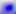

Summary:
  - Identification: Toxoplasma gondii
  - Magnification: 400x
  - Modality: photomicrograph